Give the extent of all Plasmodium parasites.
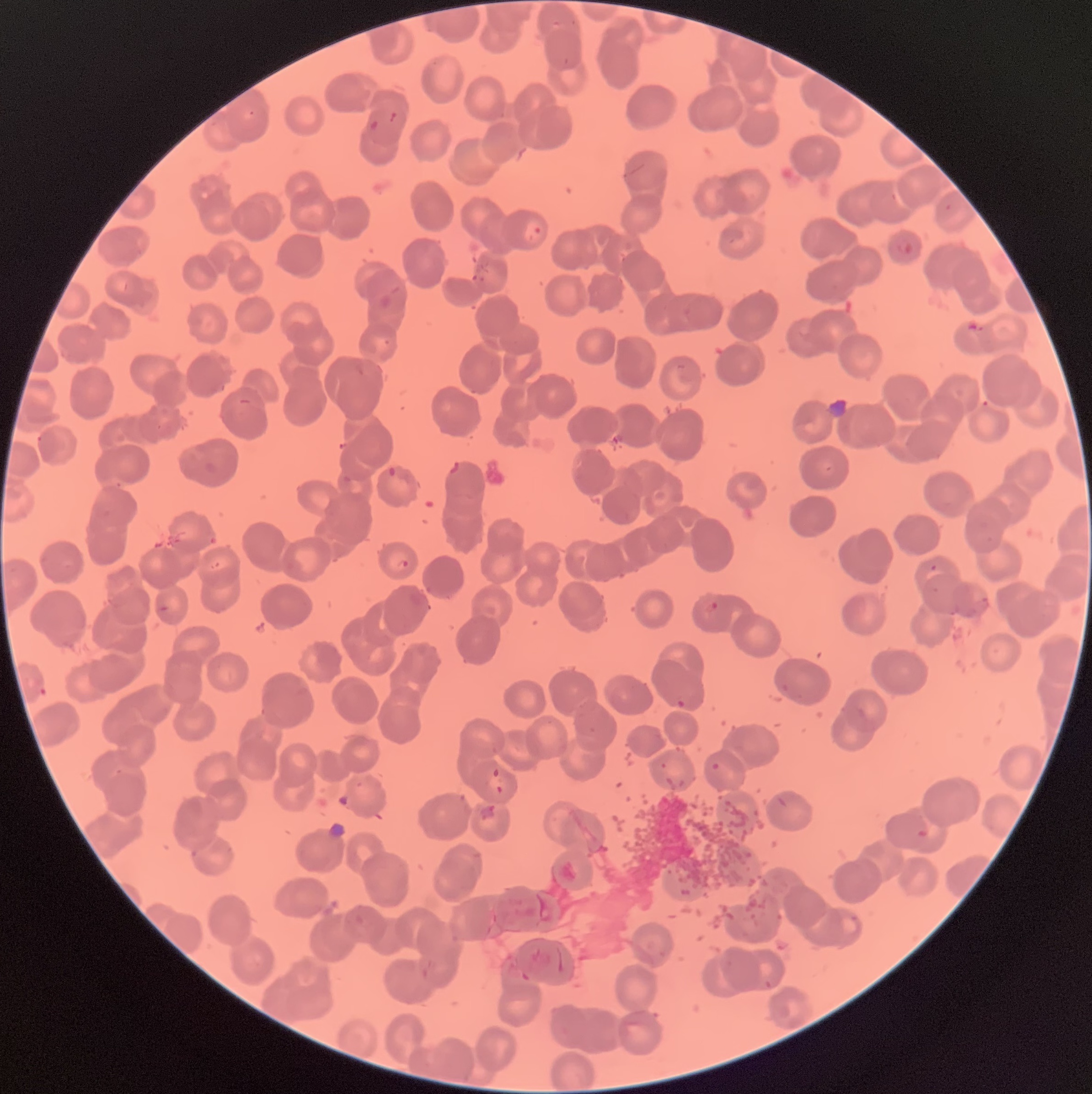
Approximate bounding boxes as (x1,y1)-(x2,y2) corner pairs in pixels.
Plasmodium parasites: (894,241)-(915,256), (471,271)-(489,283), (36,435)-(59,459), (396,559)-(408,570), (705,600)-(718,616).

Image is 1092×1094 pixels. Thin blood film. The red blood cells show rouleaux formation. Optical microscopy.